Name the blood parasite species.
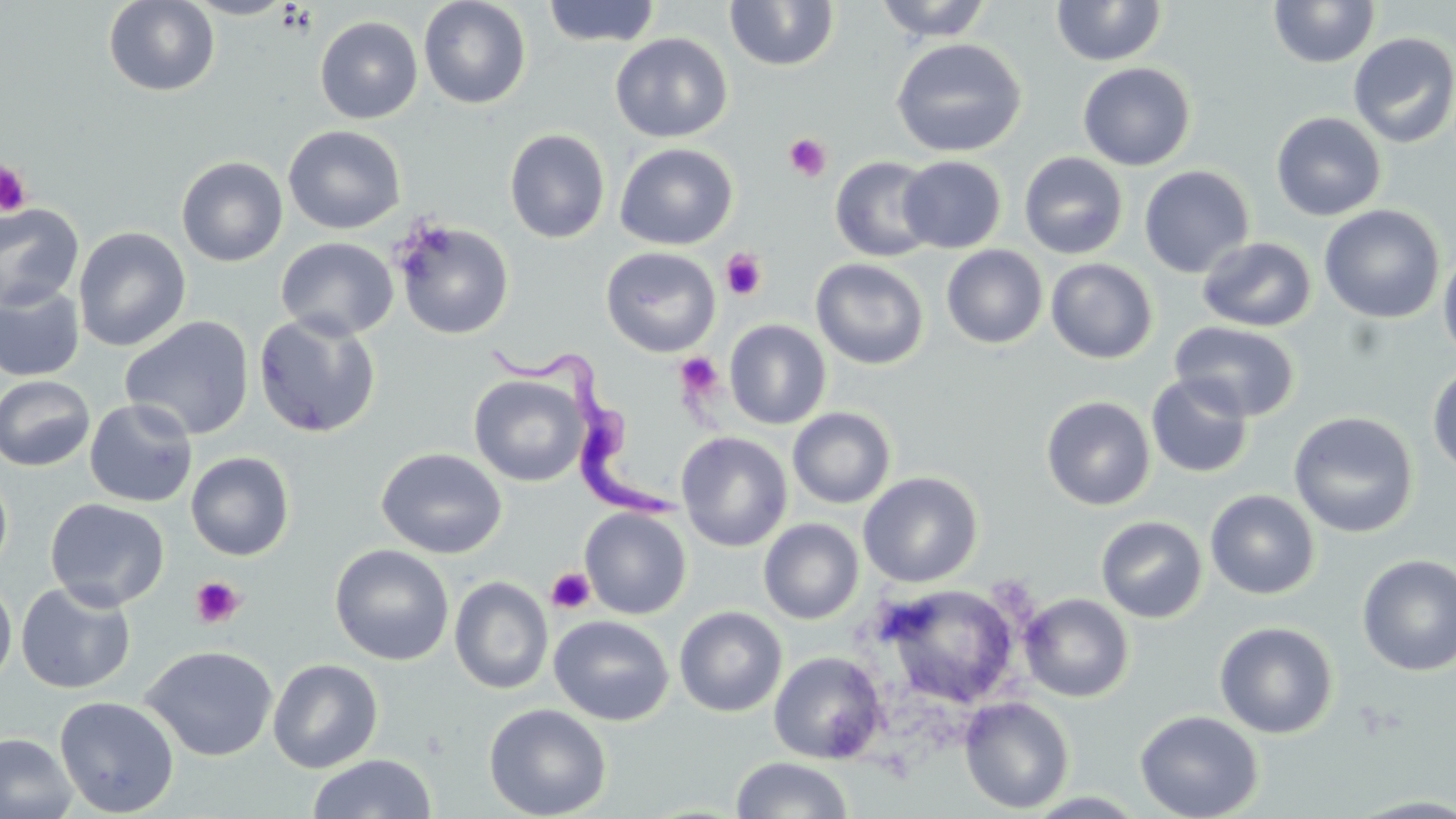

Trypanosoma brucei.

platelet locations = approximate bounding boxes as named x1/y1/x2/y2 corners in pixels: (x1=784, y1=132, x2=833, y2=182), (x1=0, y1=160, x2=33, y2=218), (x1=721, y1=249, x2=767, y2=300), (x1=675, y1=352, x2=724, y2=400), (x1=546, y1=567, x2=595, y2=615), (x1=190, y1=576, x2=245, y2=629)
field of view = one of a larger specimen
uninfected red blood cell locations = approximate bounding boxes as named x1/y1/x2/y2 corners in pixels: (x1=103, y1=0, x2=220, y2=97), (x1=183, y1=0, x2=298, y2=19), (x1=418, y1=0, x2=532, y2=110), (x1=724, y1=0, x2=840, y2=71), (x1=873, y1=0, x2=994, y2=42), (x1=1051, y1=0, x2=1168, y2=67), (x1=1268, y1=0, x2=1380, y2=68), (x1=541, y1=1, x2=662, y2=47), (x1=314, y1=16, x2=423, y2=124), (x1=1348, y1=32, x2=1456, y2=149), (x1=610, y1=33, x2=733, y2=142), (x1=890, y1=37, x2=1028, y2=159), (x1=1077, y1=62, x2=1196, y2=171), (x1=1270, y1=111, x2=1387, y2=221), (x1=283, y1=124, x2=406, y2=234), (x1=504, y1=129, x2=611, y2=244), (x1=614, y1=142, x2=738, y2=250), (x1=1018, y1=151, x2=1129, y2=259), (x1=898, y1=155, x2=1007, y2=254), (x1=175, y1=156, x2=289, y2=267), (x1=830, y1=156, x2=939, y2=262), (x1=1139, y1=165, x2=1254, y2=278), (x1=0, y1=202, x2=84, y2=312), (x1=1319, y1=204, x2=1445, y2=323), (x1=393, y1=220, x2=515, y2=340), (x1=73, y1=226, x2=191, y2=351), (x1=1197, y1=236, x2=1317, y2=332), (x1=275, y1=237, x2=399, y2=341), (x1=941, y1=245, x2=1048, y2=349), (x1=599, y1=246, x2=722, y2=357), (x1=1438, y1=249, x2=1456, y2=362), (x1=811, y1=258, x2=929, y2=370), (x1=1045, y1=258, x2=1159, y2=364), (x1=0, y1=284, x2=85, y2=382), (x1=252, y1=313, x2=382, y2=439), (x1=119, y1=315, x2=255, y2=441), (x1=724, y1=319, x2=832, y2=429), (x1=1169, y1=321, x2=1301, y2=422), (x1=1426, y1=363, x2=1456, y2=477), (x1=469, y1=373, x2=589, y2=487), (x1=1146, y1=373, x2=1254, y2=478), (x1=0, y1=374, x2=96, y2=472), (x1=1041, y1=395, x2=1155, y2=510), (x1=84, y1=398, x2=198, y2=507), (x1=787, y1=406, x2=896, y2=509), (x1=1288, y1=410, x2=1419, y2=539), (x1=676, y1=432, x2=793, y2=552), (x1=376, y1=447, x2=507, y2=559), (x1=185, y1=451, x2=295, y2=561), (x1=0, y1=466, x2=13, y2=579), (x1=858, y1=471, x2=983, y2=588), (x1=1205, y1=490, x2=1320, y2=600), (x1=45, y1=497, x2=170, y2=611), (x1=579, y1=507, x2=692, y2=619), (x1=1095, y1=516, x2=1207, y2=623), (x1=758, y1=518, x2=864, y2=624), (x1=330, y1=544, x2=454, y2=666), (x1=1356, y1=554, x2=1456, y2=676), (x1=0, y1=575, x2=17, y2=689), (x1=449, y1=576, x2=553, y2=695), (x1=15, y1=581, x2=137, y2=694), (x1=876, y1=584, x2=1021, y2=709), (x1=1020, y1=593, x2=1134, y2=702), (x1=674, y1=606, x2=788, y2=717), (x1=549, y1=615, x2=674, y2=726), (x1=1214, y1=621, x2=1338, y2=739), (x1=140, y1=644, x2=278, y2=761), (x1=769, y1=651, x2=888, y2=764), (x1=267, y1=658, x2=384, y2=773), (x1=54, y1=695, x2=179, y2=817), (x1=959, y1=695, x2=1074, y2=814), (x1=484, y1=703, x2=612, y2=819), (x1=1134, y1=709, x2=1264, y2=819), (x1=0, y1=732, x2=79, y2=819), (x1=306, y1=753, x2=437, y2=818), (x1=730, y1=756, x2=854, y2=818)
stain = May-Grünwald-Giemsa
modality = optical microscopy
preparation = thin blood film
Trypanosoma brucei locations = approximate bounding boxes as named x1/y1/x2/y2 corners in pixels: (x1=485, y1=342, x2=682, y2=523)
image size = 1456×819 pixels
magnification = 1000x